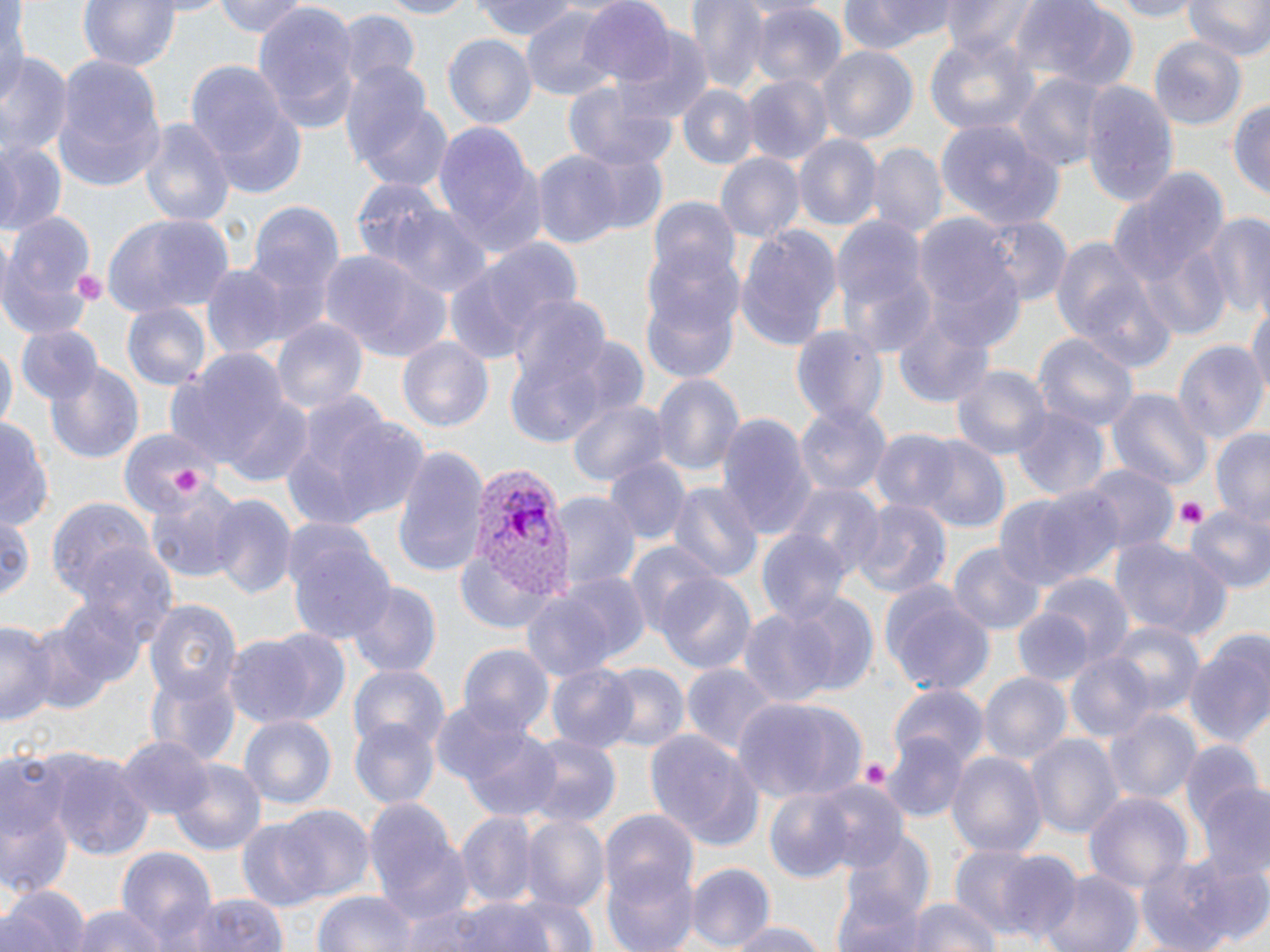
slide-level diagnosis = Plasmodium vivax
modality = light microscopy
preparation = thin blood film
platelet locations = approximate bounding boxes as [x1, y1, x2, y2] in pixels: [73, 271, 107, 300], [172, 470, 203, 497], [1173, 499, 1207, 528], [859, 760, 891, 791]
stain = May-Grünwald-Giemsa
field of view = one of a larger specimen
Plasmodium vivax-infected red blood cell locations = approximate bounding boxes as [x1, y1, x2, y2] in pixels: [465, 460, 573, 602]
image size = 1270×952 pixels
magnification = 1000x
uninfected red blood cell locations = approximate bounding boxes as [x1, y1, x2, y2] in pixels: [0, 0, 25, 117], [74, 0, 184, 71], [214, 0, 309, 38], [371, 0, 477, 18], [473, 0, 582, 41], [685, 0, 777, 94], [838, 0, 960, 55], [941, 0, 1041, 60], [1100, 0, 1205, 20], [1185, 0, 1270, 63], [578, 1, 677, 89], [750, 2, 847, 92], [1014, 2, 1141, 93], [251, 6, 358, 135], [520, 7, 620, 101], [339, 12, 420, 91], [616, 28, 716, 122], [923, 31, 1035, 138], [441, 33, 537, 130], [1149, 38, 1247, 130], [817, 46, 917, 144], [52, 52, 167, 191], [2, 56, 72, 159], [190, 66, 306, 196], [740, 73, 832, 163], [1013, 73, 1105, 172], [344, 77, 452, 191], [564, 82, 677, 169], [1080, 82, 1179, 205], [677, 84, 761, 168], [1229, 97, 1270, 206], [137, 117, 235, 230], [937, 120, 1067, 231], [432, 121, 542, 256], [794, 136, 880, 232], [0, 142, 67, 232], [868, 142, 945, 240], [565, 145, 670, 240], [530, 150, 628, 252], [716, 153, 804, 247], [1106, 162, 1228, 305], [347, 178, 457, 274], [243, 197, 342, 334], [646, 199, 742, 289], [386, 204, 495, 299], [102, 212, 234, 317], [0, 213, 99, 339], [1200, 213, 1270, 320], [830, 214, 931, 335], [912, 214, 1024, 342], [980, 216, 1070, 308], [733, 224, 843, 350], [1051, 232, 1173, 367], [479, 238, 584, 345], [643, 241, 747, 348], [1141, 247, 1230, 340], [325, 252, 456, 363], [201, 264, 290, 362], [445, 264, 542, 364], [641, 287, 740, 383], [508, 291, 611, 385], [1248, 299, 1270, 409], [120, 302, 213, 391], [893, 314, 998, 410], [270, 316, 368, 420], [791, 324, 887, 424], [14, 325, 104, 405], [1031, 330, 1141, 432], [398, 336, 494, 435], [0, 339, 14, 439], [501, 339, 619, 444], [1173, 340, 1267, 449], [170, 348, 295, 472], [43, 361, 144, 464], [952, 364, 1051, 461], [653, 374, 743, 480], [1109, 387, 1211, 494], [216, 393, 313, 488], [566, 396, 668, 486], [282, 400, 429, 530], [797, 403, 890, 500], [1014, 406, 1107, 501], [717, 413, 813, 542], [0, 414, 51, 530], [117, 425, 218, 518], [1210, 427, 1270, 528], [869, 430, 960, 516], [916, 438, 1010, 534], [392, 446, 488, 579], [607, 457, 686, 543], [1083, 465, 1177, 552], [145, 479, 246, 585], [783, 479, 883, 580], [669, 480, 761, 585], [1008, 487, 1124, 589], [550, 492, 641, 595], [210, 494, 295, 601], [48, 497, 157, 602], [850, 498, 950, 600], [1186, 505, 1270, 596], [0, 506, 36, 610], [284, 524, 395, 647], [757, 531, 852, 629], [1110, 538, 1231, 643], [623, 543, 723, 641], [948, 543, 1045, 635], [454, 550, 564, 635], [656, 574, 756, 675], [1039, 574, 1133, 669], [346, 583, 441, 677], [880, 583, 995, 695], [519, 592, 618, 683], [783, 593, 881, 699], [48, 595, 147, 695], [144, 598, 240, 704], [739, 607, 838, 710], [1010, 608, 1097, 686], [0, 620, 55, 727], [1105, 620, 1205, 714], [222, 632, 338, 727], [1183, 633, 1270, 752], [457, 645, 557, 738], [1065, 650, 1154, 741], [547, 663, 642, 753], [682, 664, 780, 757], [598, 665, 689, 755], [350, 666, 449, 755], [146, 667, 240, 767], [978, 671, 1071, 767], [889, 685, 988, 770], [735, 696, 870, 803], [440, 707, 562, 820], [1105, 708, 1201, 805], [238, 714, 337, 810], [350, 722, 439, 808], [882, 728, 972, 822], [643, 729, 762, 853], [1026, 732, 1123, 840], [522, 734, 621, 830], [118, 736, 214, 821], [1180, 744, 1265, 830], [946, 750, 1046, 862], [50, 752, 155, 863], [166, 759, 269, 858], [1, 773, 76, 903], [810, 781, 912, 881], [1198, 784, 1270, 882], [764, 786, 859, 882], [1082, 790, 1193, 899], [363, 796, 473, 928], [272, 804, 375, 901], [601, 810, 698, 900], [457, 813, 539, 909], [520, 813, 610, 920], [234, 819, 331, 913], [834, 832, 939, 931], [947, 843, 1056, 942], [117, 847, 216, 952], [601, 851, 699, 952], [994, 851, 1084, 946], [1134, 853, 1257, 949], [1187, 864, 1270, 951], [684, 865, 774, 949], [1040, 871, 1142, 952], [829, 873, 933, 952], [3, 883, 90, 952], [312, 891, 419, 952], [182, 892, 289, 952], [901, 895, 1002, 952], [402, 897, 563, 952], [64, 906, 167, 952], [720, 919, 829, 951]